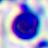
Summary:
  - Modality: micrograph
  - Magnification: 400x
  - Identification: white blood cell